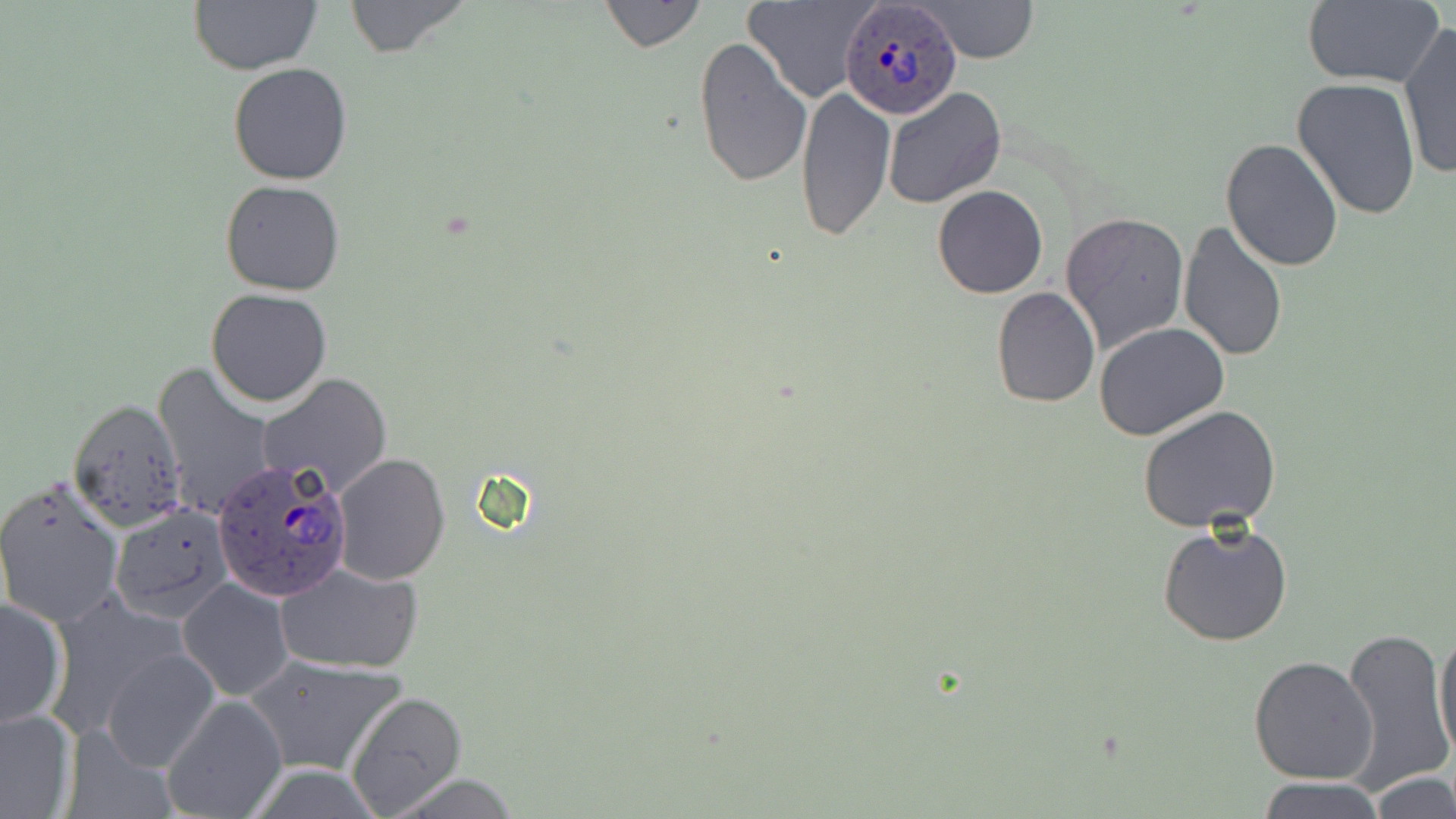
Summary:
  - Coordinate format: approximate bounding boxes as named x1/y1/x2/y2 corners in pixels
  - Plasmodium ovale-infected red blood cell locations: (x1=839, y1=2, x2=957, y2=116), (x1=209, y1=457, x2=354, y2=602)
  - Uninfected red blood cell locations: (x1=342, y1=0, x2=474, y2=57), (x1=600, y1=0, x2=705, y2=52), (x1=745, y1=0, x2=877, y2=105), (x1=915, y1=0, x2=1041, y2=63), (x1=1300, y1=0, x2=1447, y2=90), (x1=188, y1=1, x2=324, y2=75), (x1=1398, y1=23, x2=1455, y2=180), (x1=692, y1=37, x2=812, y2=189), (x1=228, y1=62, x2=353, y2=185), (x1=1292, y1=77, x2=1422, y2=220), (x1=796, y1=86, x2=895, y2=243), (x1=881, y1=86, x2=1006, y2=209), (x1=1220, y1=138, x2=1344, y2=270), (x1=219, y1=179, x2=345, y2=296), (x1=932, y1=185, x2=1048, y2=298), (x1=1060, y1=212, x2=1189, y2=356), (x1=1177, y1=220, x2=1288, y2=362), (x1=1014, y1=251, x2=1167, y2=397), (x1=991, y1=287, x2=1099, y2=407), (x1=206, y1=288, x2=331, y2=407), (x1=1094, y1=322, x2=1229, y2=441), (x1=152, y1=361, x2=274, y2=521), (x1=257, y1=373, x2=392, y2=497), (x1=67, y1=397, x2=188, y2=531), (x1=1138, y1=406, x2=1283, y2=534), (x1=334, y1=453, x2=450, y2=586), (x1=0, y1=475, x2=126, y2=629), (x1=108, y1=503, x2=233, y2=622), (x1=1158, y1=518, x2=1294, y2=646), (x1=276, y1=562, x2=424, y2=674), (x1=177, y1=577, x2=295, y2=700), (x1=43, y1=595, x2=192, y2=737), (x1=0, y1=597, x2=68, y2=729), (x1=1434, y1=623, x2=1456, y2=762), (x1=1338, y1=624, x2=1452, y2=795), (x1=100, y1=647, x2=221, y2=772), (x1=243, y1=653, x2=407, y2=777), (x1=1249, y1=655, x2=1379, y2=785), (x1=345, y1=689, x2=469, y2=817), (x1=160, y1=694, x2=287, y2=819), (x1=0, y1=708, x2=77, y2=817), (x1=1370, y1=772, x2=1456, y2=818), (x1=383, y1=773, x2=526, y2=817), (x1=1258, y1=777, x2=1385, y2=819)
  - Slide-level diagnosis: Plasmodium ovale
  - Field of view: one of a larger specimen
  - Preparation: thin blood film
  - Stain: May-Grünwald-Giemsa
  - Magnification: 1000x
  - Modality: optical microscopy
  - Image size: 1456×819 pixels